Assess this cell for malaria.
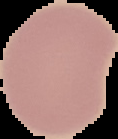

It is uninfected.

preparation = thin blood film
image size = 118×139 pixels
image type = cell region segmented out of the field of view; surrounding area masked to black